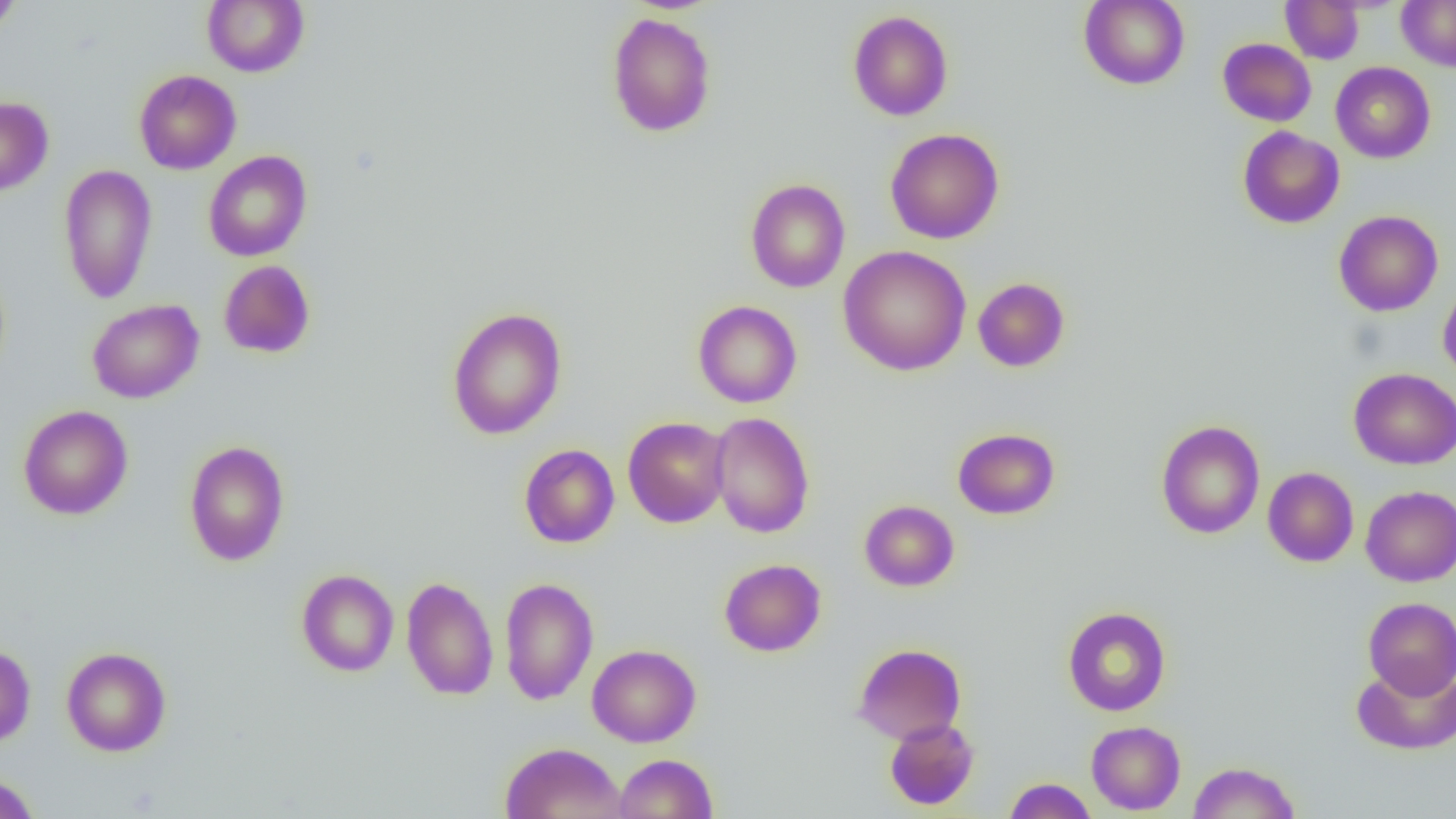
Approximate bounding boxes as named x1/y1/x2/y2 corners in pixels. Uninfected red blood cell locations: (x1=0, y1=0, x2=22, y2=35), (x1=202, y1=0, x2=309, y2=77), (x1=1079, y1=0, x2=1190, y2=90), (x1=1397, y1=0, x2=1456, y2=72), (x1=1280, y1=1, x2=1364, y2=64), (x1=848, y1=10, x2=953, y2=121), (x1=607, y1=12, x2=717, y2=137), (x1=1218, y1=38, x2=1316, y2=126), (x1=1330, y1=62, x2=1435, y2=163), (x1=134, y1=70, x2=242, y2=175), (x1=0, y1=96, x2=53, y2=197), (x1=1238, y1=126, x2=1344, y2=229), (x1=885, y1=128, x2=1004, y2=244), (x1=203, y1=150, x2=312, y2=261), (x1=58, y1=165, x2=157, y2=303), (x1=745, y1=178, x2=850, y2=293), (x1=1333, y1=210, x2=1443, y2=316), (x1=838, y1=245, x2=972, y2=376), (x1=218, y1=259, x2=316, y2=358), (x1=973, y1=277, x2=1070, y2=372), (x1=1438, y1=281, x2=1456, y2=384), (x1=86, y1=299, x2=204, y2=404), (x1=693, y1=300, x2=802, y2=407), (x1=447, y1=306, x2=567, y2=440), (x1=1349, y1=367, x2=1456, y2=470), (x1=18, y1=405, x2=133, y2=520), (x1=709, y1=411, x2=815, y2=538), (x1=622, y1=416, x2=731, y2=528), (x1=1156, y1=420, x2=1265, y2=539), (x1=952, y1=428, x2=1060, y2=520), (x1=183, y1=439, x2=290, y2=566), (x1=519, y1=443, x2=619, y2=548), (x1=1263, y1=467, x2=1358, y2=567), (x1=1360, y1=486, x2=1456, y2=586), (x1=859, y1=500, x2=959, y2=591), (x1=719, y1=558, x2=826, y2=656), (x1=296, y1=569, x2=399, y2=677), (x1=401, y1=577, x2=498, y2=700), (x1=499, y1=577, x2=599, y2=705), (x1=1363, y1=597, x2=1456, y2=699), (x1=1062, y1=606, x2=1171, y2=716), (x1=852, y1=643, x2=966, y2=745), (x1=0, y1=644, x2=36, y2=747), (x1=587, y1=644, x2=701, y2=747), (x1=61, y1=646, x2=172, y2=756), (x1=1351, y1=660, x2=1456, y2=755), (x1=884, y1=717, x2=980, y2=810), (x1=1086, y1=720, x2=1186, y2=815), (x1=499, y1=742, x2=627, y2=819), (x1=614, y1=753, x2=718, y2=818), (x1=1188, y1=761, x2=1301, y2=818), (x1=0, y1=772, x2=40, y2=819), (x1=1003, y1=777, x2=1097, y2=819). Slide-level diagnosis: negative for blood parasites. Thin blood film. Light microscopy. Captured at 1000x magnification. Image is 1456×819 pixels. Single field of view.